Locate and identify every blood parasite.
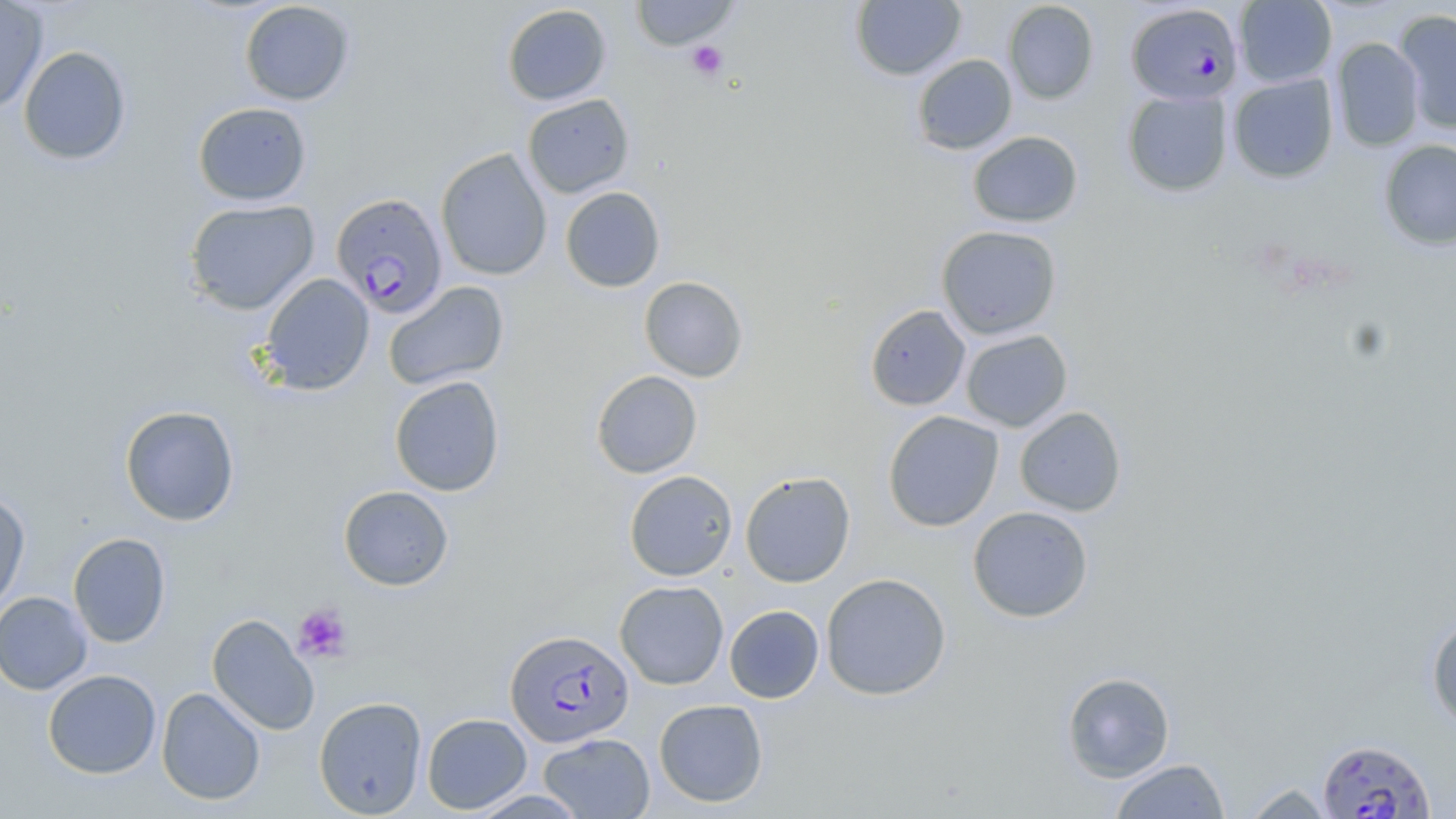
Approximate bounding boxes as (x1,y1)-(x2,y2) corner pairs in pixels.
Plasmodium falciparum-infected red blood cells: (1126,2)-(1243,105), (330,193)-(448,318), (505,629)-(634,747), (1317,738)-(1436,819).
No Plasmodium ovale, Plasmodium malariae, Plasmodium vivax, Babesia divergens, or Trypanosoma brucei observed.

Platelet locations: (686,40)-(728,80), (292,603)-(353,662). Uninfected red blood cell locations: (629,0)-(740,51), (850,0)-(966,81), (1234,0)-(1337,87), (0,1)-(49,114), (239,1)-(355,105), (1002,1)-(1099,104), (501,4)-(612,106), (1394,9)-(1456,135), (1330,37)-(1425,151), (18,45)-(132,166), (912,54)-(1018,155), (1227,73)-(1339,183), (1122,89)-(1233,197), (522,94)-(635,199), (193,102)-(311,206), (967,131)-(1083,227), (1378,140)-(1456,250), (435,148)-(553,281), (560,187)-(665,292), (183,199)-(320,315), (936,225)-(1063,340), (259,273)-(374,396), (639,276)-(749,382), (382,281)-(509,391), (865,304)-(971,411), (960,329)-(1073,432), (591,370)-(703,478), (389,376)-(505,497), (119,405)-(240,526), (1014,407)-(1127,516), (883,411)-(1004,532), (623,470)-(738,581), (740,471)-(856,587), (338,485)-(454,591), (0,491)-(31,613), (967,505)-(1094,623), (68,533)-(171,648), (821,573)-(951,701), (615,580)-(729,690), (0,591)-(93,695), (724,605)-(824,703), (207,614)-(320,735), (1426,616)-(1456,733), (43,669)-(161,779), (1062,671)-(1175,782), (156,687)-(266,806), (313,696)-(428,817), (654,699)-(768,807), (421,713)-(532,814), (538,732)-(655,818), (1108,758)-(1230,818), (1240,782)-(1336,818), (469,790)-(590,818). Slide-level diagnosis: Plasmodium falciparum. Image is 1456×819 pixels. Thin blood smear. May-Grünwald-Giemsa stain. Single field of view. Captured at 1000x magnification. Optical microscopy.